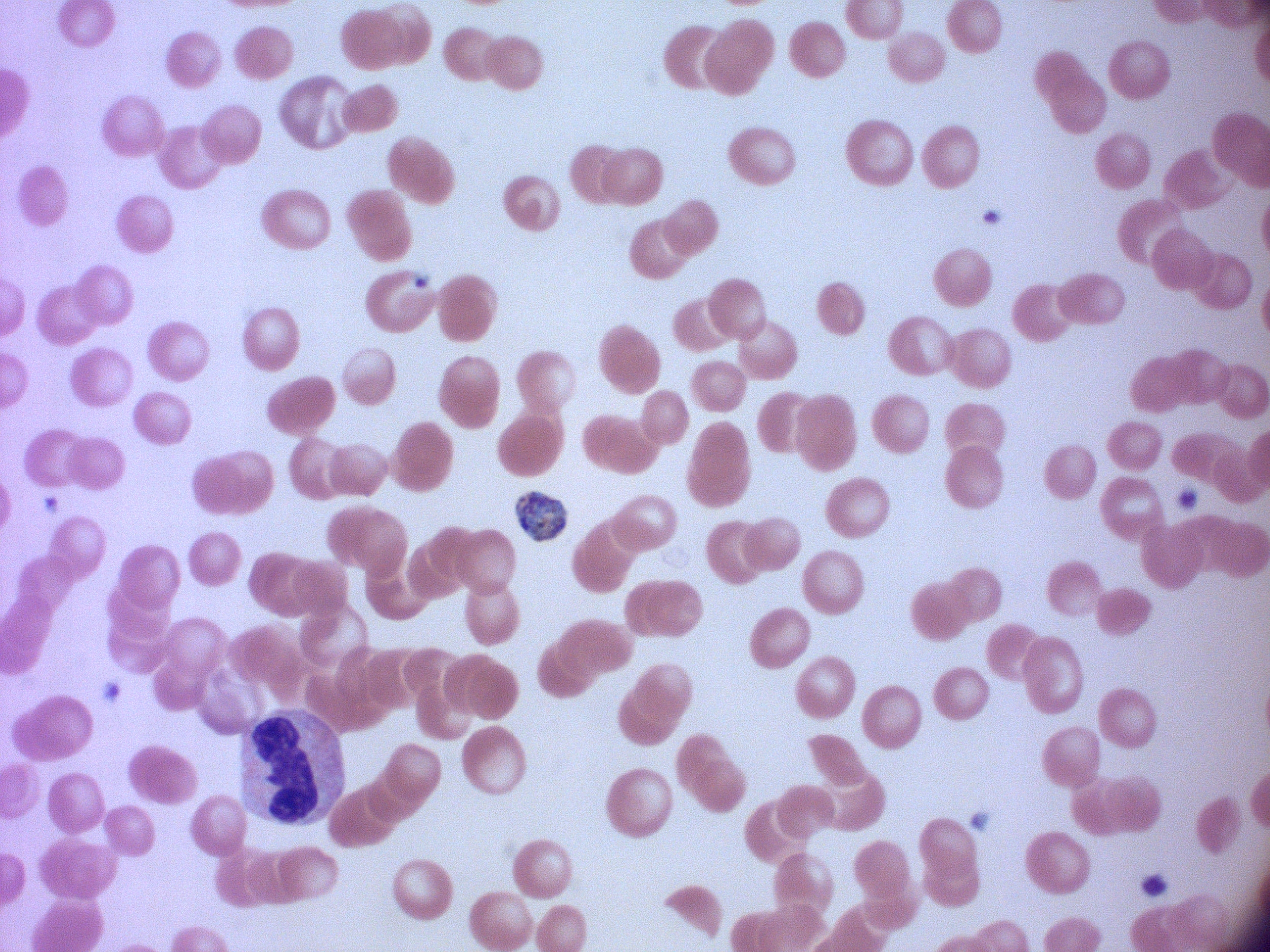
Approximate bounding boxes as (x1, y1, x2, y2) in pixels, from the source annotation, which is not necessarily exhaustive. Schizont locations: (516, 492, 566, 542). Giemsa stain. Species: Plasmodium falciparum. Image is 1270×952 pixels. Captured at 100x magnification. One field from this slide. Acquired with a Leica DM2000 optical microscope and its built-in camera. Thin blood film.